State the preparation type.
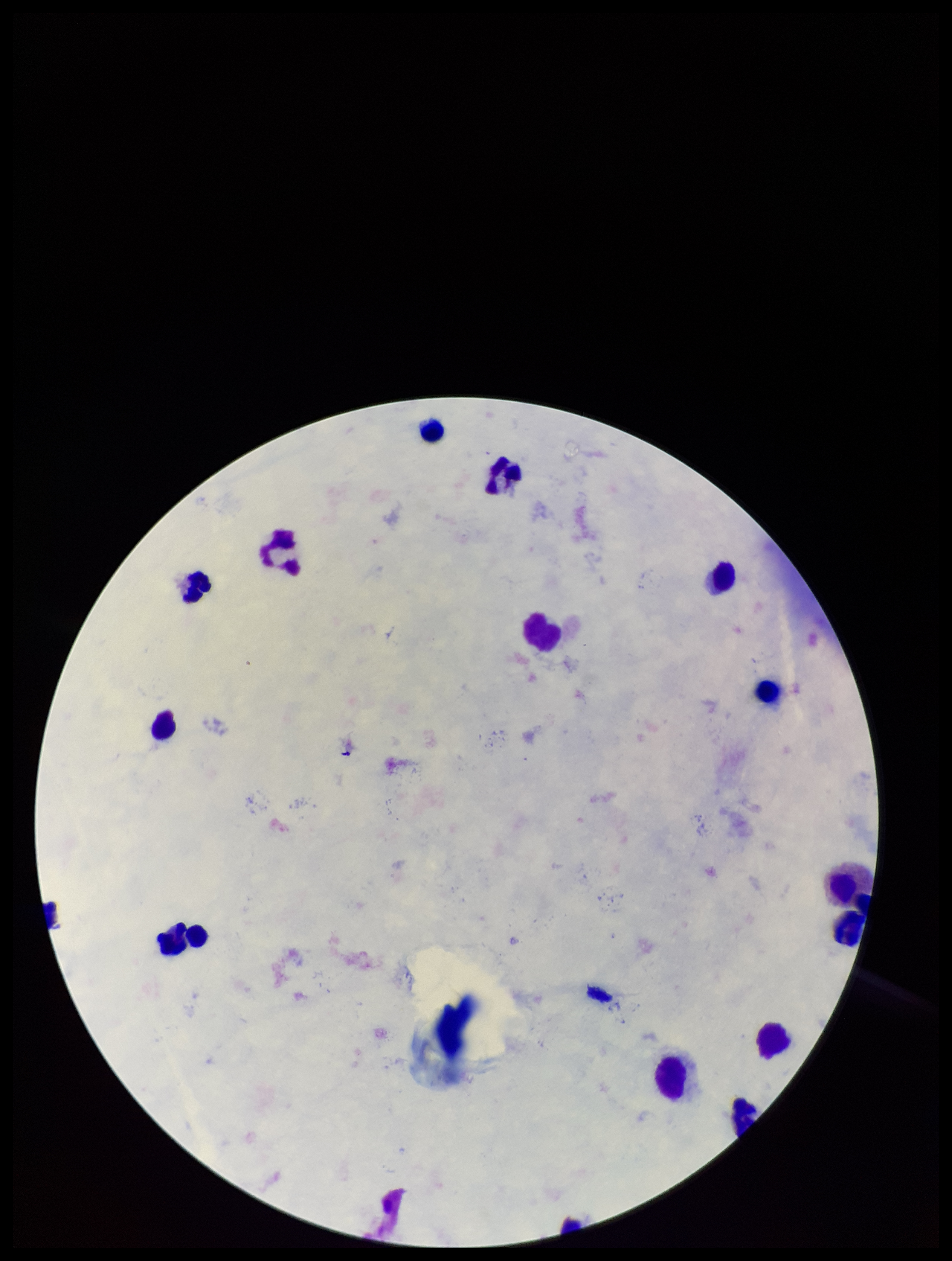

A thick smear.

{
  "leukocyte_count": 15,
  "field_of_view": "single",
  "capture": "smartphone photograph through the microscope eyepiece",
  "species_reported_for_this_patient": "Plasmodium falciparum",
  "plasmodium_parasites": "none detected",
  "image_size": "952×1261 pixels",
  "parasite_count": 0,
  "stain": "Giemsa",
  "patient_malaria_status": "positive"
}